Identify the cell.
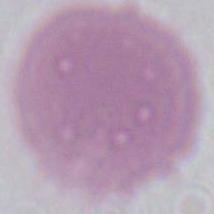

This is an erythrocyte.

1000x magnification. Photomicrograph.